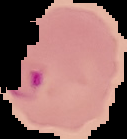

Summary:
  - Preparation: thin blood film
  - Malaria status: parasitized
  - Image type: segmented cell region on a black background
  - Image size: 127×139 pixels